Classify this cell by malaria status.
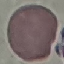
It is uninfected.

Giemsa stain. Thin blood film. Automatically extracted cell patch, resized to 64 × 64 pixels. Acquired by smartphone through the microscope eyepiece.